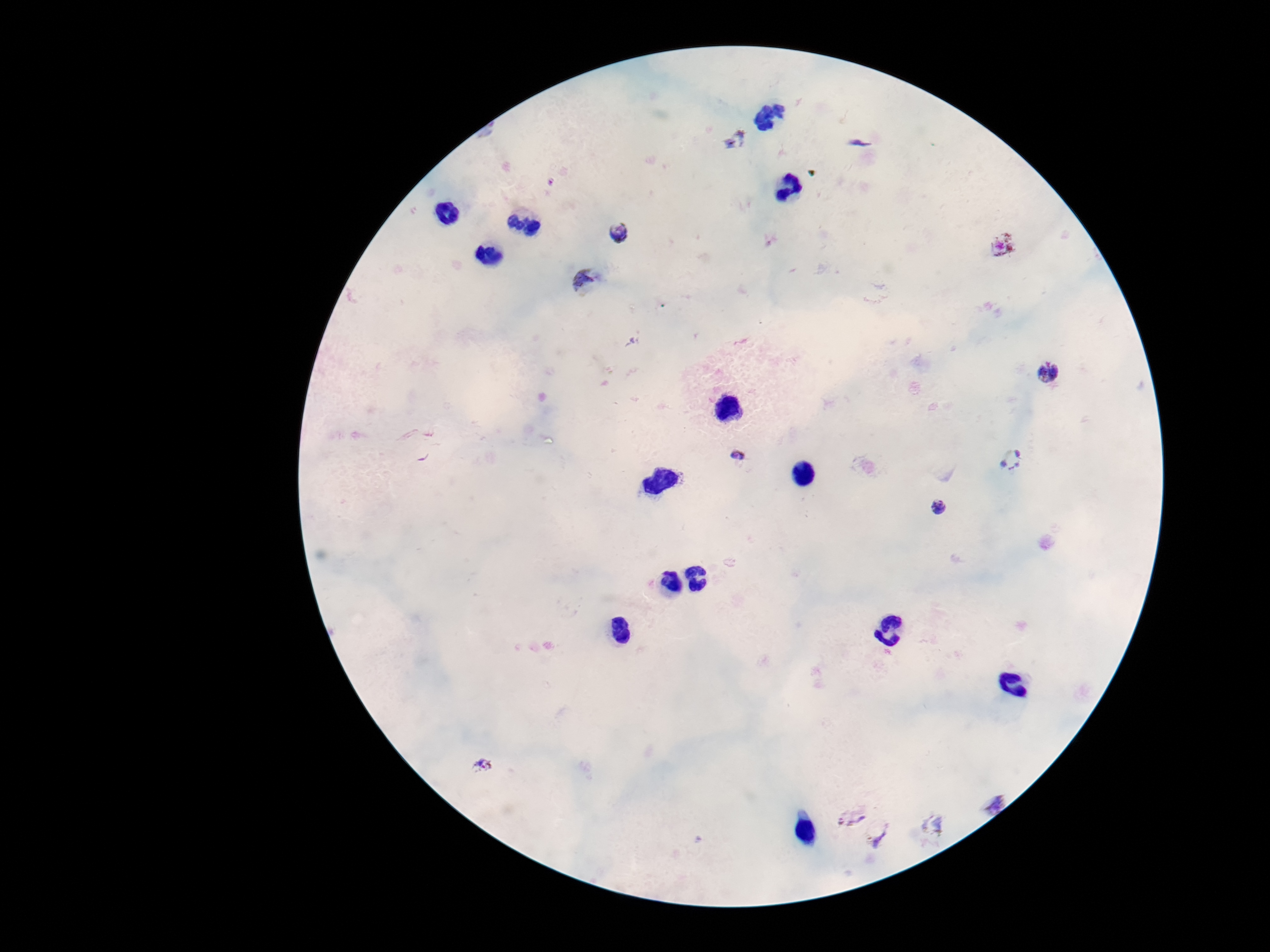
Approximate centers as (x, y) in pixels. Plasmodium parasite locations: (736, 139), (618, 232), (1005, 244), (585, 281), (1047, 372), (738, 454), (1010, 459), (939, 507), (482, 765), (992, 800), (848, 815), (931, 824), (879, 834). Smartphone photograph taken through the microscope eyepiece. Image is 1270×952 pixels. Patient malaria status: infected. 100x magnification. Giemsa stain. Thick peripheral-blood smear. Single field of view.